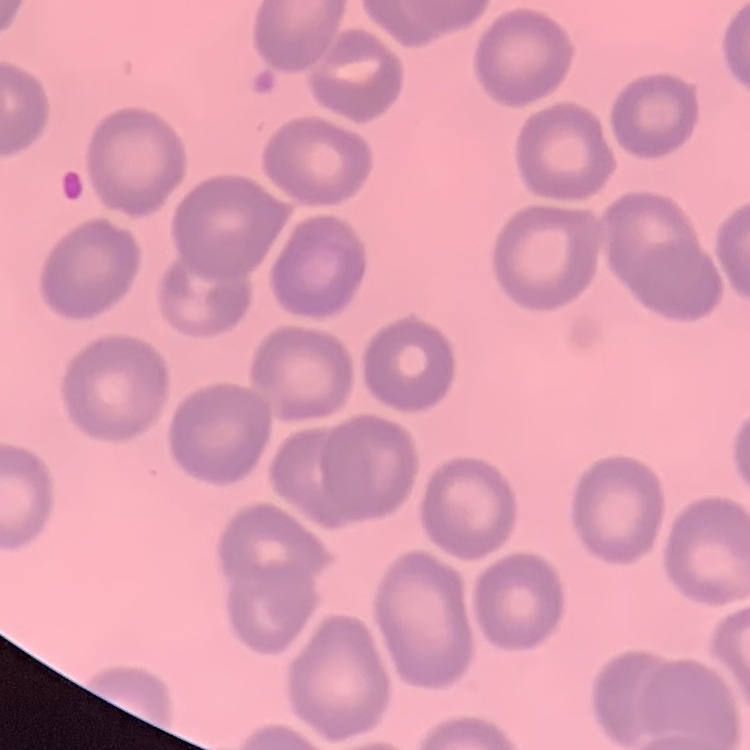
{
  "red_blood_cell_morphology": "no rouleaux formation",
  "stain": "Field's or Giemsa",
  "preparation": "thin blood smear",
  "image_type": "square crop of a larger photomicrograph"
}